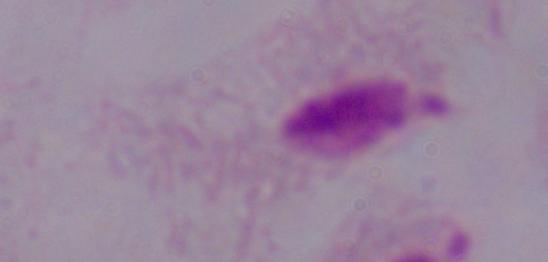

magnification = 1000x
identification = trichomonad
modality = micrograph